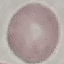
malaria status = uninfected
preparation = thin smear
image type = automatically extracted cell patch, resized to 64 × 64 pixels
capture = smartphone through the microscope eyepiece
stain = Giemsa